State the blood parasite species.
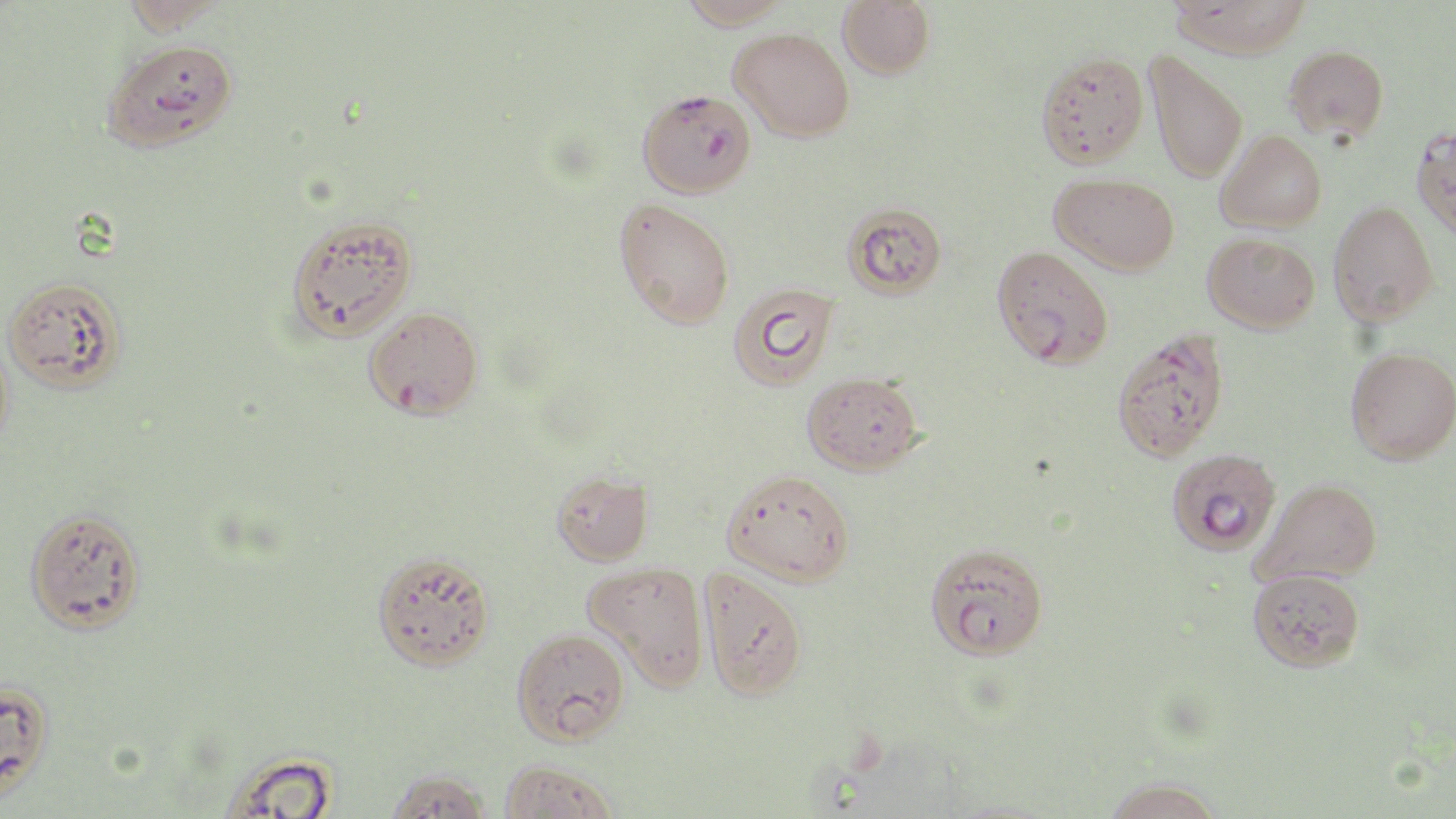

Plasmodium falciparum.

Summary:
  - Coordinate format: approximate bounding boxes as (x1, y1, x2, y2) in pixels
  - Uninfected red blood cell locations: (121, 0, 232, 35), (674, 0, 795, 30), (837, 0, 935, 79), (1168, 0, 1313, 58), (730, 28, 855, 142), (101, 38, 238, 153), (1284, 45, 1389, 141), (1036, 51, 1149, 167), (1145, 51, 1248, 184), (1412, 125, 1456, 241), (1216, 130, 1327, 233), (1051, 173, 1179, 275), (614, 198, 735, 329), (1328, 201, 1440, 327), (843, 202, 948, 298), (284, 213, 418, 342), (1203, 233, 1320, 333), (2, 275, 127, 393), (727, 282, 839, 391), (0, 333, 16, 453), (1346, 347, 1456, 464), (802, 371, 923, 475), (722, 469, 855, 585), (552, 471, 653, 565), (1254, 478, 1382, 586), (24, 505, 147, 634), (924, 543, 1048, 660), (372, 550, 495, 671), (583, 562, 710, 690), (699, 566, 809, 701), (1248, 568, 1364, 672), (512, 627, 630, 745), (0, 679, 55, 805), (213, 749, 343, 819), (499, 759, 620, 819), (384, 768, 495, 818), (1101, 777, 1225, 819)
  - Plasmodium falciparum-infected red blood cell locations: (637, 88, 757, 198), (991, 245, 1114, 368), (363, 305, 484, 420), (1111, 329, 1229, 461), (1169, 451, 1284, 558)
  - Magnification: 1000x
  - Stain: May-Grünwald-Giemsa
  - Modality: optical microscopy
  - Image size: 1456×819 pixels
  - Field of view: one of a larger specimen
  - Preparation: thin blood film